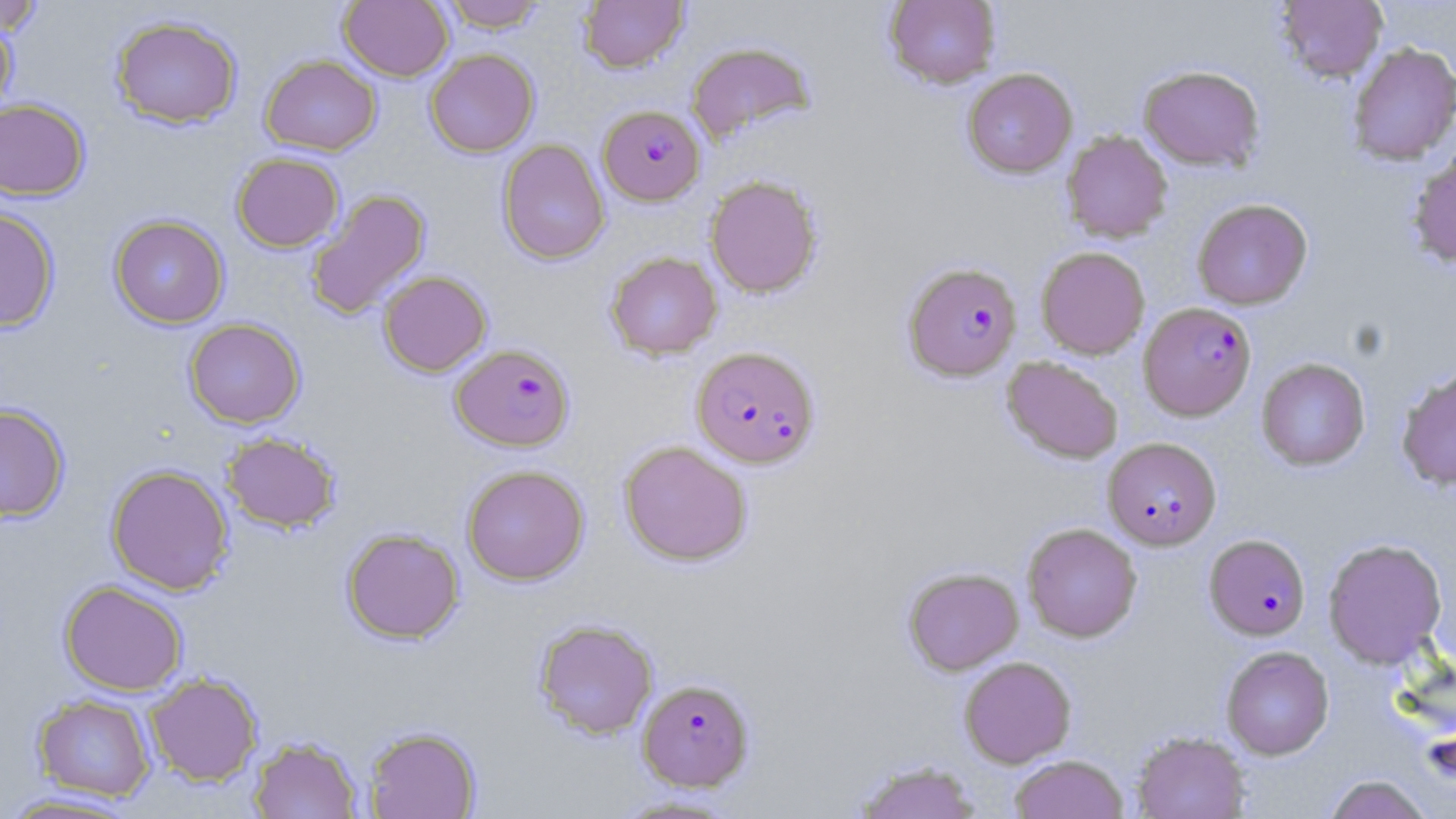

Summary:
  - Coordinate format: approximate bounding boxes as named x1/y1/x2/y2 corners in pixels
  - Plasmodium falciparum-infected red blood cell locations: (x1=598, y1=105, x2=706, y2=205), (x1=903, y1=262, x2=1022, y2=381), (x1=1139, y1=302, x2=1256, y2=420), (x1=451, y1=344, x2=574, y2=451), (x1=692, y1=346, x2=819, y2=468), (x1=1103, y1=437, x2=1222, y2=549), (x1=1204, y1=534, x2=1310, y2=640), (x1=637, y1=678, x2=755, y2=792)
  - Uninfected red blood cell locations: (x1=339, y1=0, x2=453, y2=81), (x1=438, y1=0, x2=548, y2=31), (x1=578, y1=0, x2=688, y2=73), (x1=884, y1=0, x2=1001, y2=88), (x1=1274, y1=0, x2=1388, y2=83), (x1=0, y1=2, x2=47, y2=36), (x1=110, y1=15, x2=243, y2=129), (x1=0, y1=18, x2=17, y2=121), (x1=686, y1=41, x2=815, y2=144), (x1=1347, y1=42, x2=1456, y2=165), (x1=424, y1=48, x2=539, y2=157), (x1=261, y1=55, x2=381, y2=155), (x1=1139, y1=64, x2=1264, y2=170), (x1=962, y1=68, x2=1077, y2=177), (x1=0, y1=98, x2=90, y2=200), (x1=1061, y1=130, x2=1173, y2=243), (x1=497, y1=139, x2=609, y2=265), (x1=1407, y1=150, x2=1456, y2=269), (x1=231, y1=152, x2=344, y2=252), (x1=705, y1=175, x2=822, y2=297), (x1=305, y1=189, x2=430, y2=320), (x1=1192, y1=198, x2=1312, y2=310), (x1=0, y1=206, x2=60, y2=331), (x1=109, y1=214, x2=229, y2=328), (x1=1036, y1=246, x2=1150, y2=359), (x1=605, y1=251, x2=722, y2=359), (x1=378, y1=271, x2=491, y2=376), (x1=184, y1=318, x2=305, y2=428), (x1=1002, y1=356, x2=1124, y2=464), (x1=1256, y1=357, x2=1370, y2=470), (x1=1396, y1=366, x2=1456, y2=491), (x1=0, y1=403, x2=70, y2=522), (x1=221, y1=432, x2=341, y2=533), (x1=619, y1=441, x2=753, y2=566), (x1=106, y1=464, x2=234, y2=595), (x1=461, y1=464, x2=589, y2=585), (x1=1022, y1=523, x2=1142, y2=642), (x1=342, y1=528, x2=464, y2=643), (x1=1323, y1=537, x2=1447, y2=668), (x1=903, y1=567, x2=1023, y2=675), (x1=59, y1=580, x2=188, y2=695), (x1=533, y1=618, x2=659, y2=739), (x1=1221, y1=646, x2=1334, y2=759), (x1=959, y1=656, x2=1076, y2=767), (x1=144, y1=672, x2=263, y2=786), (x1=32, y1=693, x2=156, y2=802), (x1=363, y1=725, x2=482, y2=818), (x1=1131, y1=730, x2=1250, y2=819), (x1=249, y1=735, x2=363, y2=818), (x1=1010, y1=754, x2=1129, y2=819), (x1=854, y1=760, x2=982, y2=818), (x1=1324, y1=774, x2=1433, y2=819), (x1=0, y1=791, x2=147, y2=818), (x1=610, y1=794, x2=745, y2=818)
  - Slide-level diagnosis: Plasmodium falciparum
  - Magnification: 1000x
  - Stain: May-Grünwald-Giemsa
  - Modality: optical microscopy
  - Preparation: thin blood film
  - Field of view: single
  - Image size: 1456×819 pixels